Report the malaria status of this cell.
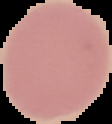

It is uninfected.

preparation = thin blood smear
image type = segmented cell region on a black background
image size = 112×124 pixels